Locate and identify every blood parasite.
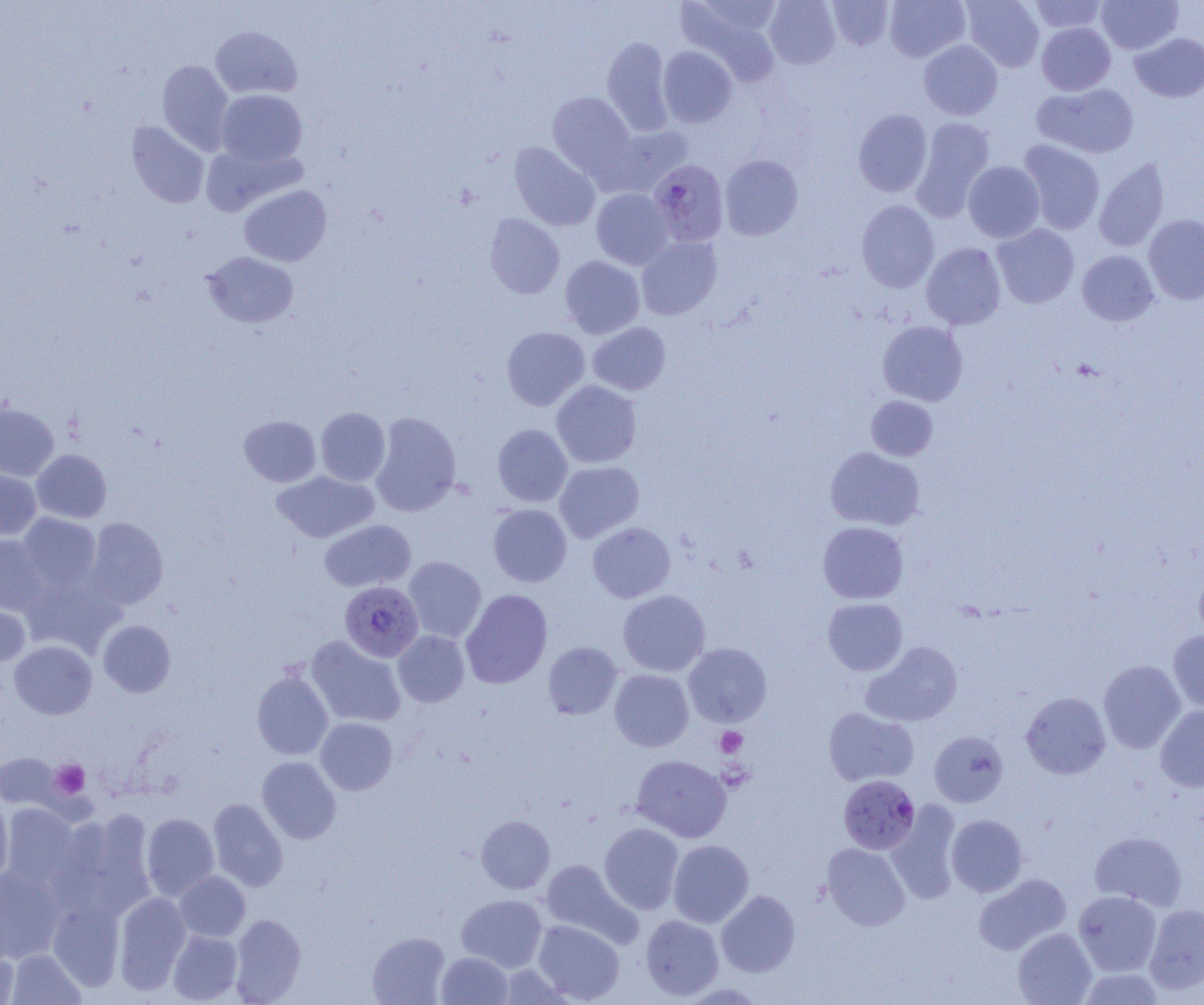
Approximate bounding boxes as [x1, y1, x2, y2] in pixels.
Plasmodium falciparum-infected red blood cells: [649, 160, 729, 246], [340, 581, 423, 661], [838, 775, 919, 854].
No Plasmodium ovale, Plasmodium malariae, Plasmodium vivax, Babesia divergens, or Trypanosoma brucei observed.

slide-level diagnosis = Plasmodium falciparum
preparation = thin blood smear
platelet locations = approximate bounding boxes as [x1, y1, x2, y2] in pixels: [715, 727, 747, 757], [717, 759, 755, 793], [51, 760, 90, 799]
magnification = 1000x
uninfected red blood cell locations = approximate bounding boxes as [x1, y1, x2, y2] in pixels: [765, 0, 840, 69], [827, 0, 894, 50], [885, 0, 970, 62], [961, 0, 1044, 71], [1029, 0, 1108, 33], [1096, 0, 1182, 54], [677, 2, 782, 85], [1037, 22, 1115, 95], [210, 26, 302, 99], [1130, 33, 1204, 103], [602, 36, 673, 136], [919, 40, 1002, 120], [658, 46, 737, 127], [157, 60, 233, 154], [1034, 83, 1139, 158], [216, 89, 307, 168], [547, 91, 635, 178], [853, 108, 933, 197], [911, 117, 995, 220], [126, 121, 209, 209], [606, 125, 693, 196], [1019, 140, 1105, 234], [509, 141, 600, 231], [720, 155, 803, 240], [1093, 158, 1170, 252], [963, 161, 1045, 242], [239, 185, 332, 267], [591, 188, 672, 269], [856, 200, 939, 293], [485, 212, 565, 299], [1143, 214, 1204, 304], [992, 224, 1079, 308], [636, 235, 722, 320], [921, 242, 1006, 329], [1077, 250, 1158, 326], [203, 252, 298, 328], [560, 255, 645, 338], [877, 320, 968, 406], [587, 322, 671, 395], [501, 327, 589, 411], [551, 380, 641, 468], [866, 396, 937, 460], [0, 403, 59, 481], [316, 407, 390, 486], [370, 411, 461, 517], [239, 415, 320, 487], [493, 424, 573, 507], [825, 447, 925, 530], [32, 449, 111, 523], [554, 460, 644, 543], [0, 469, 41, 539], [273, 470, 379, 543], [488, 504, 572, 587], [17, 513, 101, 591], [84, 517, 168, 610], [319, 519, 416, 592], [818, 521, 908, 604], [587, 522, 676, 602], [0, 534, 48, 615], [404, 556, 486, 643], [1194, 568, 1204, 643], [20, 574, 122, 657], [460, 589, 553, 688], [618, 589, 710, 676], [823, 598, 907, 675], [0, 599, 30, 667], [99, 620, 175, 697], [1168, 629, 1204, 712], [393, 630, 469, 707], [306, 636, 406, 727], [9, 640, 97, 719], [543, 641, 622, 719], [863, 642, 962, 727], [683, 643, 771, 727], [1099, 660, 1185, 753], [609, 669, 693, 751], [251, 671, 333, 760], [1021, 692, 1111, 779], [1155, 705, 1204, 792], [823, 707, 918, 787], [315, 717, 397, 795], [929, 730, 1008, 807], [0, 753, 61, 810], [631, 755, 731, 842], [257, 756, 341, 844], [0, 796, 13, 884], [208, 799, 288, 891], [886, 802, 962, 904], [2, 803, 79, 889], [67, 811, 157, 919], [141, 813, 219, 900], [946, 814, 1028, 897], [476, 815, 555, 894], [599, 823, 684, 914], [1090, 831, 1187, 911], [668, 839, 754, 927], [822, 843, 910, 930], [540, 859, 642, 947], [0, 867, 65, 963], [175, 871, 250, 942], [973, 874, 1071, 955], [716, 890, 800, 977], [1073, 890, 1162, 976], [114, 892, 191, 994], [456, 894, 548, 972], [48, 901, 125, 992], [1144, 904, 1204, 995], [229, 914, 305, 1004], [640, 915, 724, 1000], [533, 920, 624, 1003], [1012, 928, 1097, 1005], [168, 931, 242, 1004], [367, 932, 449, 1004], [7, 949, 84, 1005], [0, 950, 19, 1004], [437, 951, 513, 1004], [1078, 969, 1167, 1005]
modality = light microscopy
image size = 1204×1005 pixels
field of view = one of a larger specimen